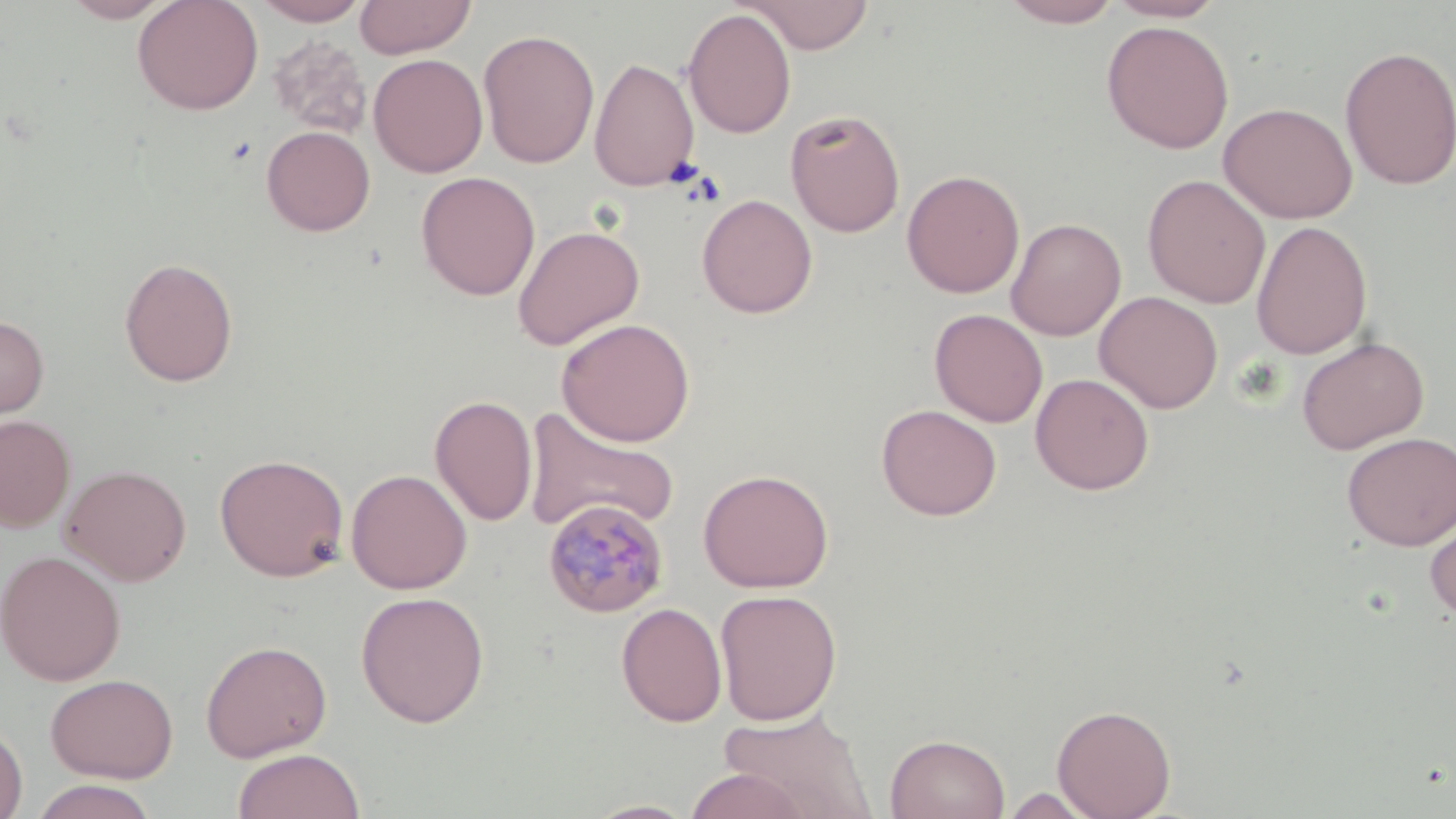

Approximate bounding boxes as named x1/y1/x2/y2 corners in pixels. Plasmodium malariae-infected red blood cell locations: (x1=541, y1=499, x2=669, y2=619). Uninfected red blood cell locations: (x1=61, y1=0, x2=174, y2=23), (x1=133, y1=0, x2=263, y2=115), (x1=252, y1=0, x2=370, y2=26), (x1=354, y1=0, x2=476, y2=59), (x1=741, y1=0, x2=875, y2=54), (x1=999, y1=0, x2=1124, y2=27), (x1=1104, y1=0, x2=1227, y2=22), (x1=682, y1=7, x2=797, y2=140), (x1=1101, y1=20, x2=1235, y2=154), (x1=479, y1=28, x2=600, y2=169), (x1=266, y1=35, x2=372, y2=140), (x1=1339, y1=45, x2=1456, y2=190), (x1=368, y1=53, x2=488, y2=178), (x1=589, y1=57, x2=700, y2=192), (x1=1219, y1=101, x2=1358, y2=224), (x1=784, y1=109, x2=906, y2=237), (x1=261, y1=125, x2=376, y2=236), (x1=901, y1=169, x2=1025, y2=298), (x1=416, y1=171, x2=541, y2=301), (x1=1142, y1=174, x2=1271, y2=309), (x1=697, y1=193, x2=818, y2=318), (x1=1006, y1=217, x2=1127, y2=341), (x1=1251, y1=219, x2=1373, y2=360), (x1=512, y1=225, x2=645, y2=350), (x1=118, y1=257, x2=239, y2=387), (x1=1094, y1=291, x2=1223, y2=413), (x1=929, y1=308, x2=1049, y2=427), (x1=0, y1=314, x2=49, y2=420), (x1=556, y1=318, x2=695, y2=447), (x1=1296, y1=336, x2=1429, y2=454), (x1=1030, y1=373, x2=1154, y2=495), (x1=429, y1=395, x2=538, y2=527), (x1=876, y1=404, x2=1002, y2=521), (x1=523, y1=406, x2=681, y2=536), (x1=0, y1=414, x2=75, y2=532), (x1=1341, y1=432, x2=1456, y2=551), (x1=214, y1=453, x2=350, y2=582), (x1=60, y1=463, x2=192, y2=586), (x1=345, y1=468, x2=472, y2=594), (x1=697, y1=468, x2=834, y2=593), (x1=1425, y1=512, x2=1456, y2=622), (x1=0, y1=549, x2=126, y2=687), (x1=714, y1=589, x2=842, y2=726), (x1=355, y1=591, x2=490, y2=727), (x1=616, y1=602, x2=727, y2=727), (x1=200, y1=639, x2=333, y2=763), (x1=44, y1=673, x2=178, y2=783), (x1=1052, y1=703, x2=1176, y2=819), (x1=717, y1=707, x2=877, y2=818), (x1=0, y1=718, x2=28, y2=819), (x1=885, y1=733, x2=1010, y2=819), (x1=232, y1=747, x2=365, y2=819), (x1=684, y1=768, x2=812, y2=819), (x1=27, y1=779, x2=162, y2=819), (x1=1000, y1=787, x2=1101, y2=818), (x1=584, y1=800, x2=701, y2=819). Slide-level diagnosis: Plasmodium malariae. One field of a larger specimen. Light microscopy. Thin blood smear. Image is 1456×819 pixels. May-Grünwald-Giemsa stain. Captured at 1000x magnification.